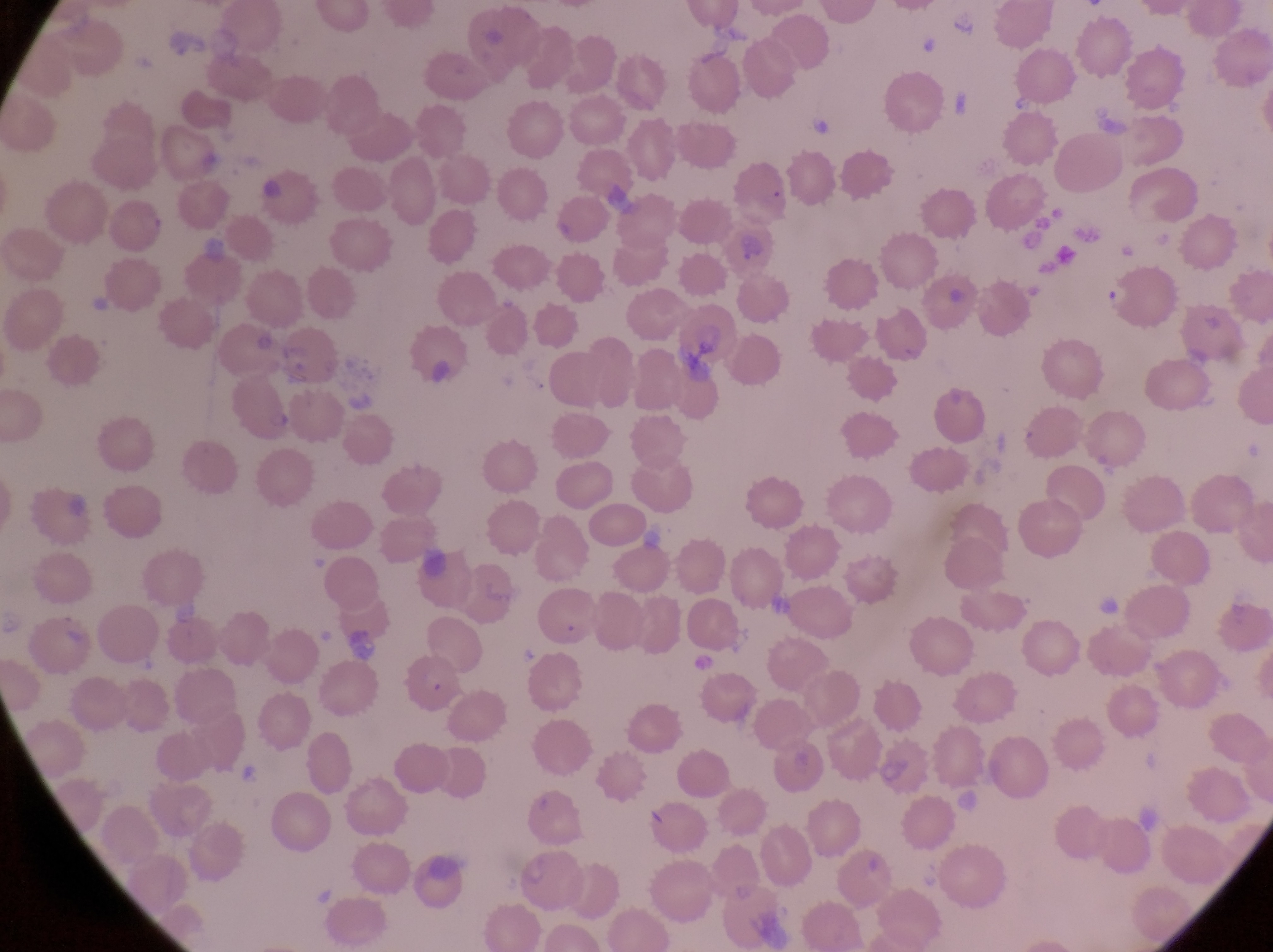 Approximate bounding boxes as {left, top, right, bottom} in pixels. Parasitised red blood cell locations: {1096, 267, 1175, 328}, {224, 370, 296, 444}, {404, 657, 465, 712}. Single field of view. Thin blood smear. Sample from Uganda. Photographed through the eyepiece of an Olympus CX-23 microscope with a smartphone camera. Image is 1273×952 pixels. Magnification of 1000x.